Locate every malaria parasite.
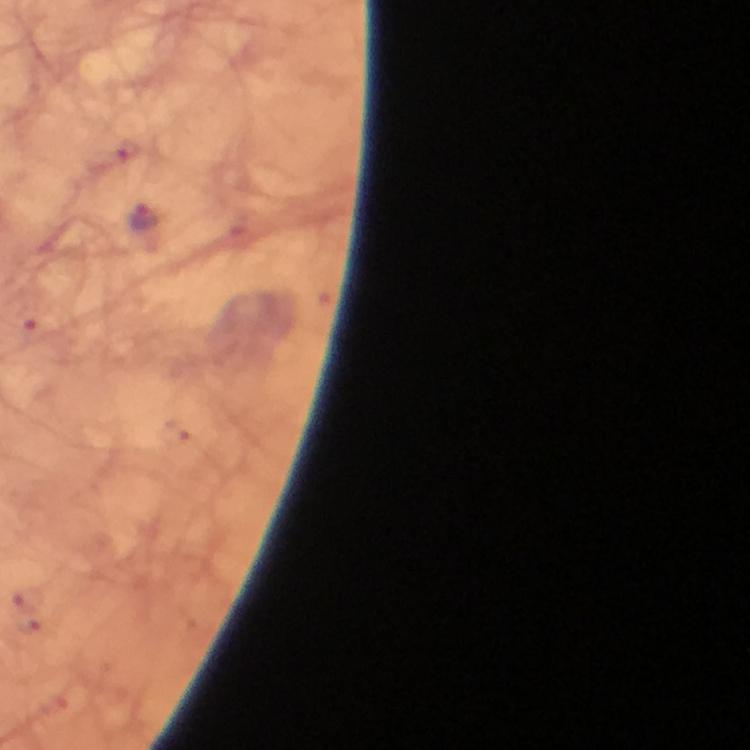
Approximate centers as (x, y) in pixels.
Malaria parasites: (145, 218).

capture: smartphone photograph through a microscope
stain: Giemsa
preparation: thick blood smear
cropped_from: one field of view
magnification: 100x
context: from a malaria diagnostic workup
image_size: 750×750 pixels
immersion_oil: applied